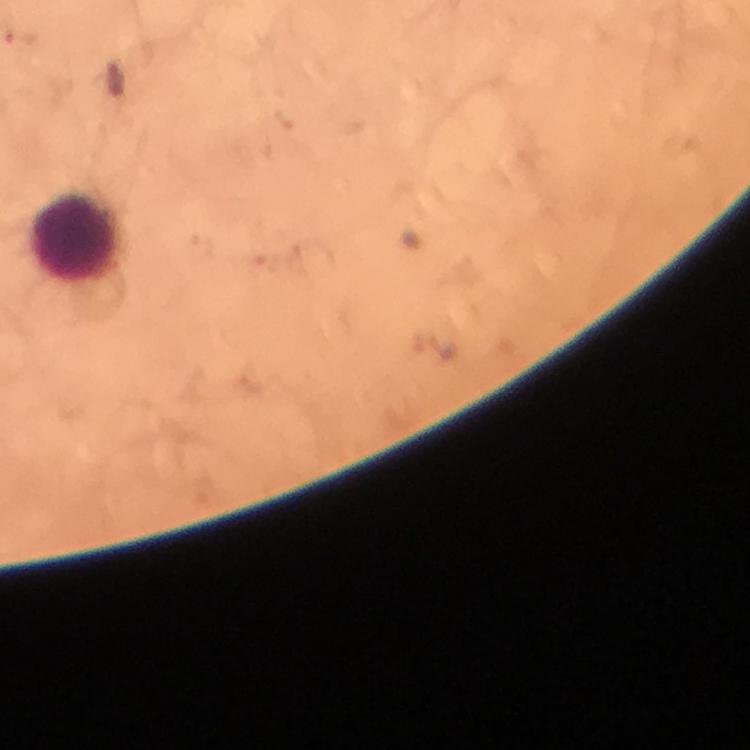
Approximate centers as [x, y] in pixels. Leukocyte locations: [74, 237]. Photographed with a smartphone mounted on the microscope. From a malaria diagnostic workup. Immersion oil was used. A crop from one field of view. Image is 750×750 pixels. Malaria parasites: none seen. Giemsa-stained preparation. At 100x magnification. Thick blood film.